Name the parasite shown.
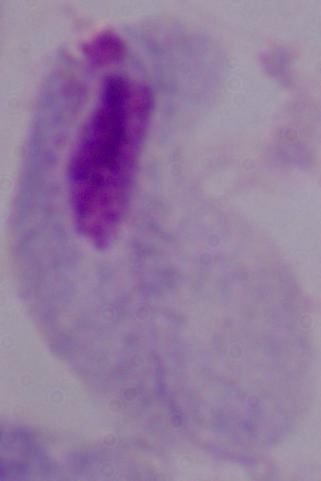
A trichomonad.

Summary:
  - Magnification: 1000x
  - Modality: photomicrograph